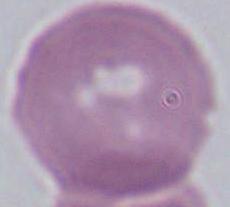

A red blood cell is shown. 1000x magnification. Micrograph.